Report the malaria status of this cell.
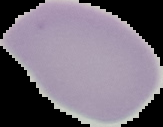

It is uninfected.

Summary:
  - Preparation: thin blood film
  - Image type: cell region segmented out of the field of view; surrounding area masked to black
  - Image size: 163×127 pixels